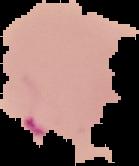

Summary:
  - Preparation: thin blood film
  - Malaria status: parasitized
  - Image type: segmented cell region on a black background
  - Image size: 139×166 pixels